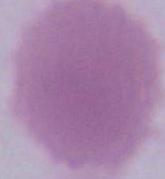

modality: photomicrograph
magnification: 1000x
identification: red blood cell